Assess this cell for malaria.
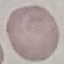
It is uninfected.

Summary:
  - Preparation: thin blood smear
  - Stain: Giemsa
  - Capture: smartphone camera at the microscope eyepiece
  - Image type: automatically extracted cell patch, resized to 64 × 64 pixels